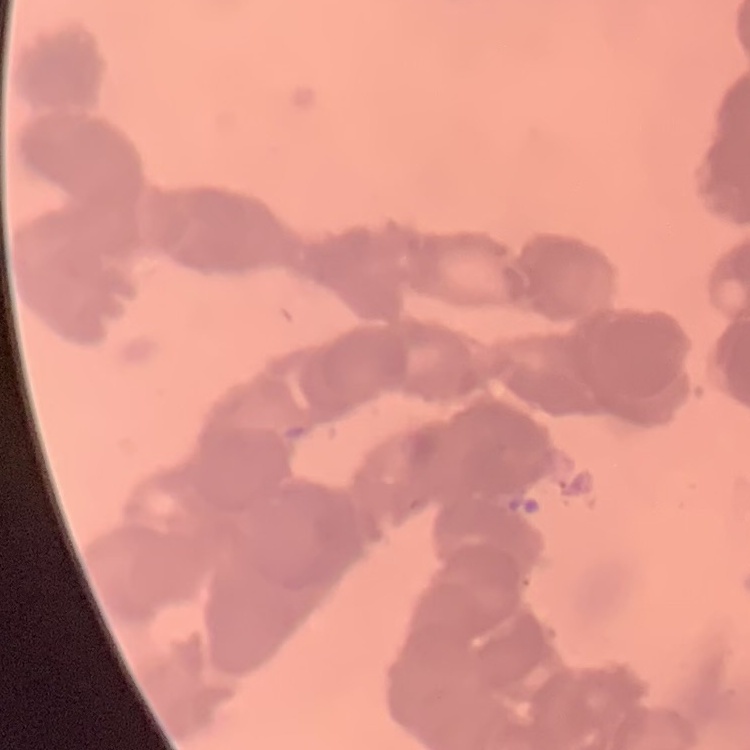
Summary:
  - Erythrocyte morphology: rouleaux formation
  - Preparation: thin blood film
  - Stain: Field's or Giemsa
  - Image type: one tile cut from a larger photomicrograph